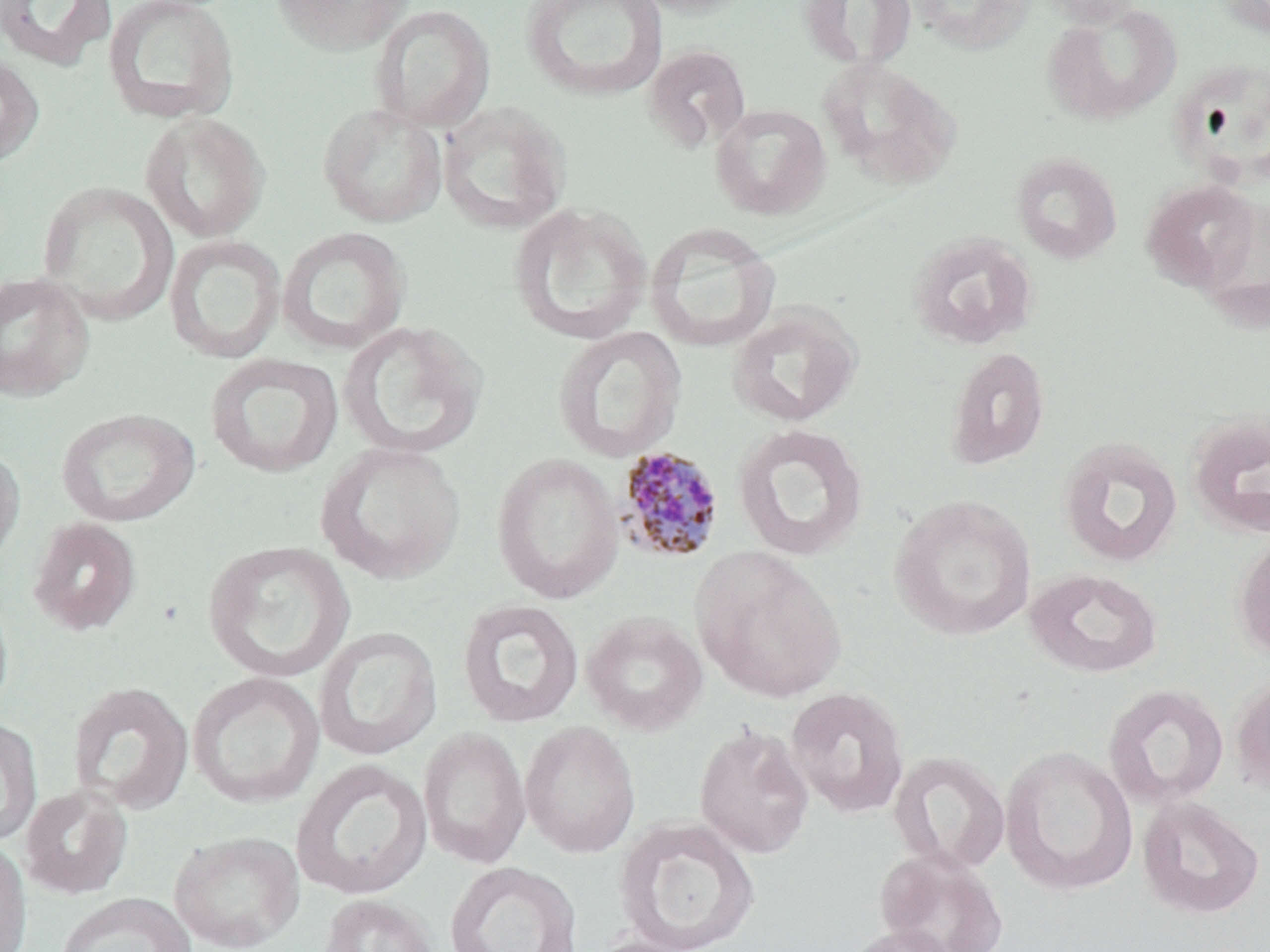

Summary:
  - Coordinate format: approximate bounding boxes as [x1, y1, x2, y2] in pixels
  - Uninfected red blood cell locations: [0, 0, 119, 72], [269, 0, 414, 55], [519, 0, 669, 103], [631, 0, 756, 18], [797, 0, 917, 72], [907, 0, 1036, 55], [1032, 0, 1147, 27], [1217, 0, 1270, 39], [101, 1, 241, 125], [1040, 2, 1183, 127], [370, 3, 495, 133], [642, 43, 751, 154], [0, 50, 44, 168], [816, 56, 962, 191], [1169, 56, 1270, 187], [317, 102, 448, 229], [437, 102, 571, 236], [710, 103, 831, 220], [138, 111, 270, 243], [1011, 151, 1123, 265], [1140, 178, 1261, 293], [35, 181, 179, 324], [1195, 197, 1270, 332], [509, 201, 653, 345], [645, 222, 781, 352], [277, 226, 411, 354], [906, 231, 1039, 351], [164, 234, 287, 364], [0, 272, 95, 402], [727, 303, 863, 428], [337, 320, 488, 462], [552, 325, 688, 463], [944, 346, 1051, 471], [205, 352, 344, 478], [56, 407, 200, 528], [1186, 411, 1270, 540], [731, 422, 869, 562], [1057, 436, 1184, 568], [315, 441, 467, 585], [0, 444, 26, 569], [491, 452, 624, 605], [889, 494, 1037, 642], [26, 516, 142, 636], [1234, 531, 1270, 661], [202, 540, 355, 684], [691, 547, 848, 703], [1023, 567, 1163, 679], [0, 587, 14, 720], [456, 598, 585, 729], [580, 611, 709, 736], [313, 626, 443, 761], [186, 671, 325, 809], [1229, 672, 1270, 796], [67, 681, 194, 815], [1102, 683, 1229, 810], [785, 686, 910, 819], [0, 715, 43, 849], [519, 721, 641, 858], [693, 722, 814, 860], [418, 727, 532, 869], [1000, 745, 1138, 896], [888, 750, 1011, 876], [290, 758, 433, 901], [19, 784, 134, 899], [1136, 795, 1265, 919], [614, 816, 761, 952], [168, 830, 305, 952], [0, 836, 32, 952], [875, 847, 1008, 952], [444, 861, 583, 952], [54, 892, 197, 952], [317, 893, 439, 952], [841, 923, 962, 952], [586, 936, 707, 952]
  - Plasmodium malariae-infected red blood cell locations: [614, 446, 725, 563]
  - Slide-level diagnosis: Plasmodium malariae
  - Image size: 1270×952 pixels
  - Stain: May-Grünwald-Giemsa
  - Magnification: 1000x
  - Modality: light microscopy
  - Preparation: thin blood film
  - Field of view: single